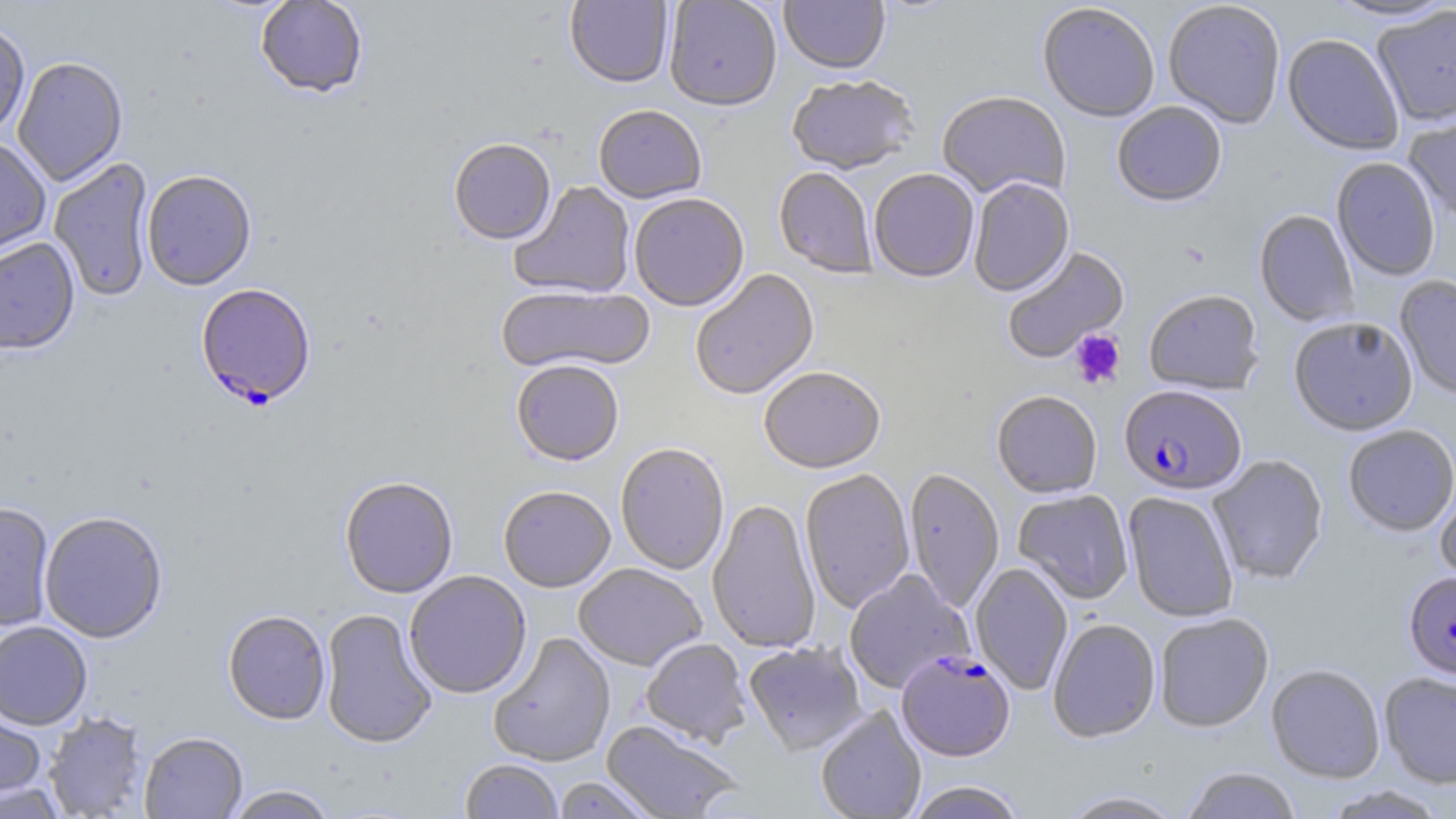
Approximate bounding boxes as [x1, y1, x2, y2] in pixels. Plasmodium falciparum-infected red blood cell locations: [196, 284, 317, 410], [1119, 385, 1247, 495], [1404, 572, 1456, 682], [896, 650, 1015, 762]. Platelet locations: [1069, 329, 1126, 388]. Uninfected red blood cell locations: [255, 0, 368, 98], [565, 0, 673, 89], [664, 0, 781, 113], [779, 0, 890, 76], [1324, 0, 1455, 23], [1162, 2, 1286, 130], [1037, 3, 1160, 124], [1371, 5, 1456, 128], [0, 20, 30, 139], [1282, 34, 1404, 157], [12, 57, 128, 187], [786, 77, 919, 177], [937, 92, 1070, 203], [1112, 102, 1227, 209], [594, 106, 706, 205], [1403, 111, 1456, 226], [0, 137, 51, 259], [448, 141, 556, 246], [49, 158, 156, 303], [1331, 158, 1440, 281], [774, 168, 876, 279], [869, 170, 979, 284], [142, 171, 257, 291], [968, 179, 1074, 297], [509, 182, 636, 300], [629, 196, 749, 312], [1254, 210, 1360, 327], [0, 237, 80, 356], [1001, 246, 1130, 365], [690, 269, 820, 401], [1395, 276, 1456, 401], [496, 285, 654, 376], [1144, 290, 1264, 397], [1289, 317, 1419, 436], [511, 361, 624, 467], [759, 368, 885, 475], [992, 391, 1102, 499], [1343, 425, 1456, 537], [615, 443, 730, 575], [1208, 455, 1328, 585], [904, 468, 1004, 613], [800, 469, 915, 614], [339, 476, 458, 599], [1435, 479, 1456, 596], [498, 486, 616, 593], [1013, 490, 1133, 605], [1122, 492, 1239, 622], [707, 499, 821, 654], [0, 502, 55, 631], [39, 511, 168, 643], [970, 562, 1073, 696], [573, 563, 706, 671], [843, 570, 975, 695], [404, 571, 532, 699], [319, 608, 438, 749], [223, 610, 331, 725], [1155, 613, 1273, 733], [1048, 618, 1161, 743], [0, 621, 93, 730], [488, 632, 616, 768], [641, 638, 751, 747], [743, 641, 867, 755], [1266, 665, 1385, 783], [1379, 673, 1456, 788], [0, 701, 48, 804], [815, 706, 926, 819], [43, 712, 148, 818], [601, 720, 744, 819], [139, 731, 248, 819], [460, 760, 563, 819], [1181, 766, 1302, 819], [553, 776, 660, 818], [0, 780, 69, 818], [905, 781, 1027, 819], [224, 786, 338, 818], [1321, 786, 1449, 818], [1057, 790, 1187, 818]. Slide-level diagnosis: Plasmodium falciparum. Thin blood smear. Image is 1456×819 pixels. Single field of view. Light microscopy. May-Grünwald-Giemsa-stained preparation. Captured at 1000x magnification.